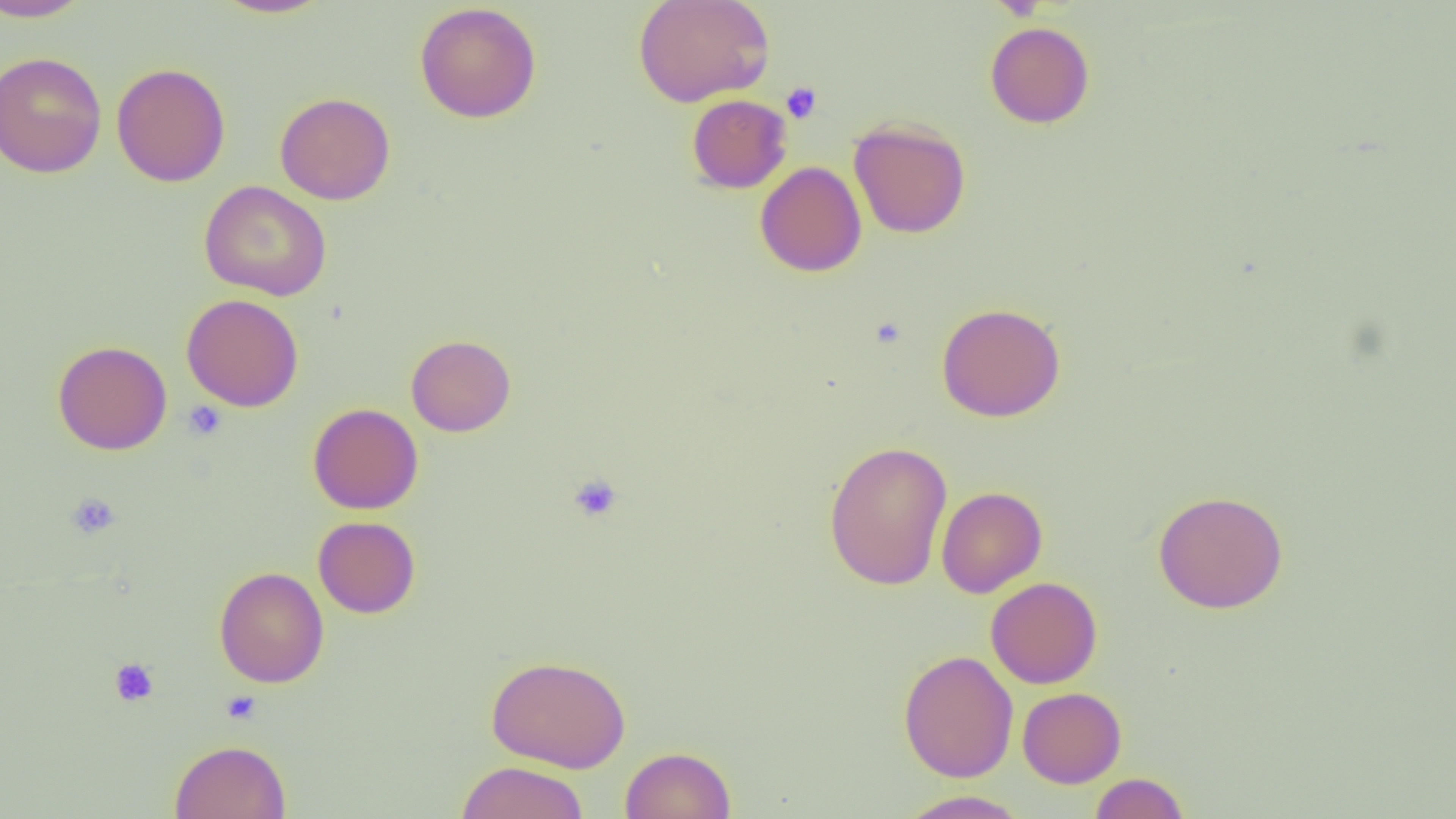
Approximate bounding boxes as [x1, y1, x2, y2] in pixels. Platelet locations: [781, 82, 821, 123], [182, 400, 227, 440], [568, 474, 622, 523], [66, 492, 121, 539], [109, 658, 159, 706], [221, 690, 262, 724]. Uninfected red blood cell locations: [0, 0, 93, 22], [210, 0, 335, 19], [633, 0, 775, 107], [413, 3, 542, 123], [985, 21, 1095, 129], [0, 51, 107, 179], [112, 62, 231, 187], [275, 92, 395, 205], [686, 94, 792, 193], [848, 118, 971, 238], [755, 161, 867, 277], [200, 180, 332, 301], [182, 294, 304, 412], [936, 302, 1066, 422], [405, 334, 516, 437], [52, 340, 172, 455], [307, 403, 423, 514], [823, 440, 952, 590], [936, 486, 1047, 598], [1152, 489, 1289, 614], [313, 516, 420, 618], [214, 566, 329, 688], [986, 577, 1102, 689], [898, 650, 1019, 782], [485, 654, 631, 773], [1018, 687, 1126, 788], [169, 739, 291, 819], [620, 746, 737, 819], [454, 761, 589, 819], [1088, 772, 1190, 819], [896, 790, 1032, 818]. Slide-level diagnosis: no evidence of blood parasites. 1000x magnification. Thin blood film. Image is 1456×819 pixels. One field of a larger specimen. Light microscopy.